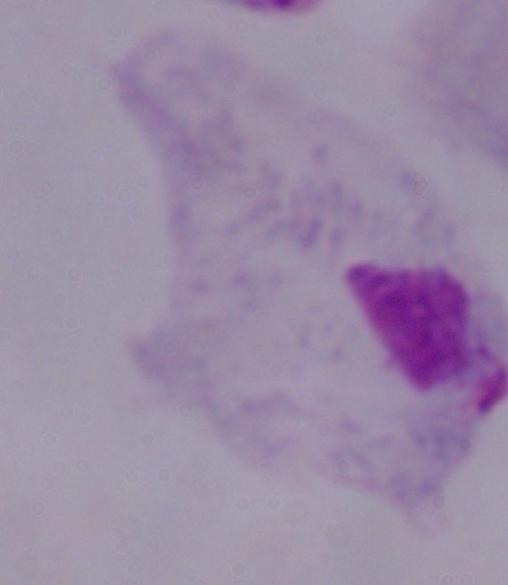

Summary:
  - Magnification: 1000x
  - Identification: trichomonad
  - Modality: photomicrograph